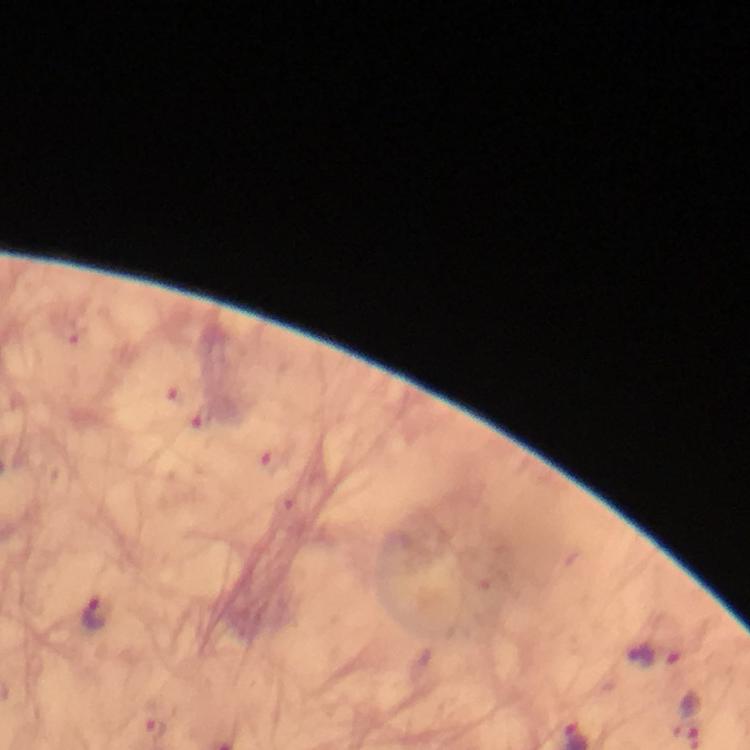
Approximate centers as {x, y} in pixels. Malaria parasite locations: {214, 418}, {98, 614}, {655, 656}. From a malaria diagnostic workup. Thick smear. Photographed with a smartphone mounted on the microscope. Image is 750×750 pixels. Giemsa-stained preparation. Immersion oil applied. 100x magnification. A crop from one field of view.